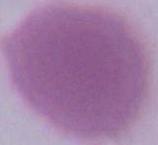

modality = photomicrograph
magnification = 1000x
identification = red blood cell